Report the malaria status of this cell.
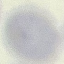
Uninfected.

stain = Giemsa
image type = automatically extracted cell patch, resized to 64 × 64 pixels
capture = smartphone camera at the microscope eyepiece
preparation = thin blood film